Assess this cell for malaria.
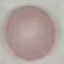
It is uninfected.

image type = automatically extracted cell patch, resized to 64 × 64 pixels
preparation = thin blood film
capture = smartphone through the microscope eyepiece
stain = Giemsa